Identify the parasite.
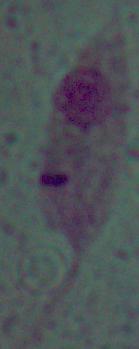
This is Leishmania.

modality = micrograph
magnification = 1000x